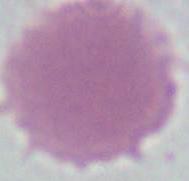
modality = photomicrograph
identification = erythrocyte
magnification = 1000x